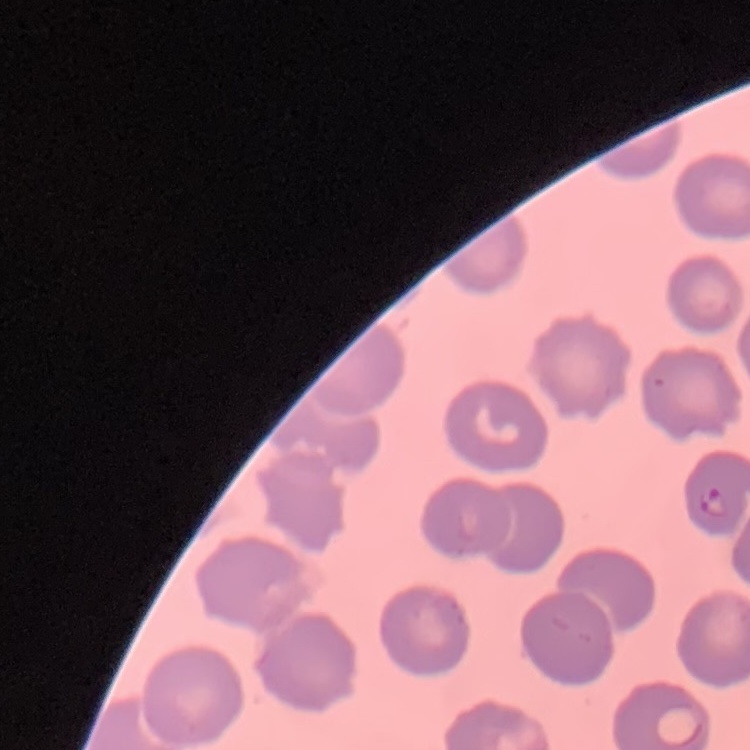

Summary:
  - Erythrocyte morphology: no rouleaux formation
  - Stain: Field's or Giemsa
  - Preparation: thin blood smear
  - Image type: square crop of a larger photomicrograph